State which parasite is depicted.
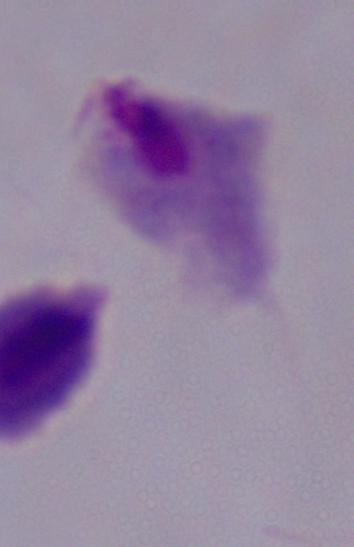
A trichomonad.

1000x magnification. Photomicrograph.